Report the malaria status of this cell.
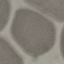
It is uninfected.

Giemsa-stained preparation. Thin blood smear. Photographed with a smartphone camera at the microscope eyepiece. Automatically extracted cell patch, resized to 64 × 64 pixels.